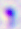

Captured at 400x magnification. Photomicrograph. Toxoplasma gondii is seen.